Comment on the morphology of the red blood cells.
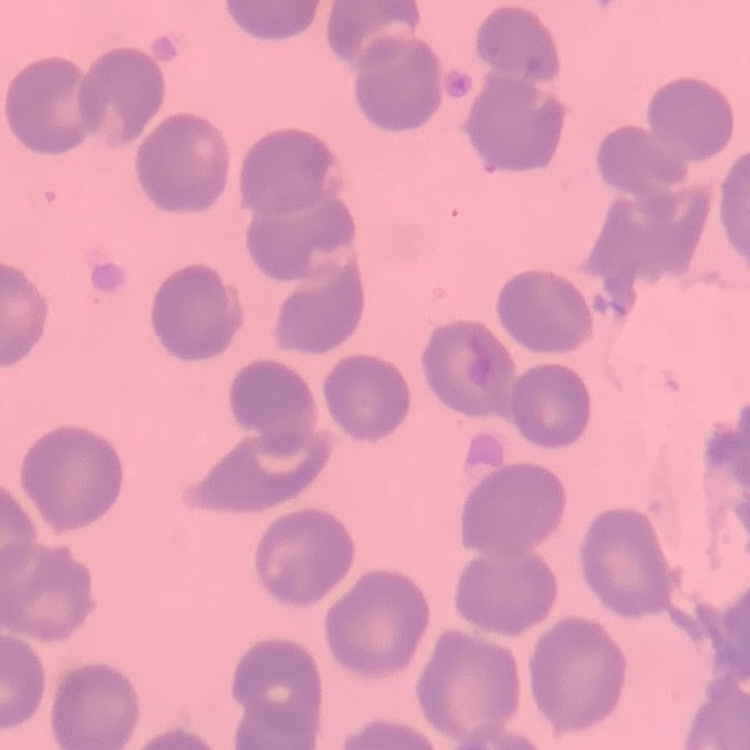
They show no rouleaux formation.

Square crop of a larger photomicrograph. Stained with either Field's or Giemsa. Thin peripheral smear.